Comment on the morphology of the red blood cells.
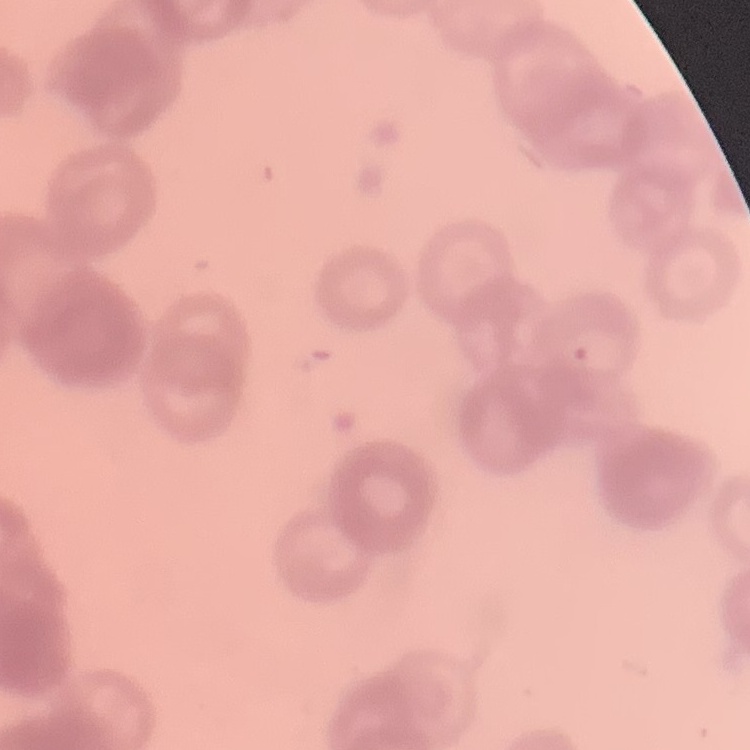

They show rouleaux formation.

Summary:
  - Image type: square crop of a larger photomicrograph
  - Stain: Field's or Giemsa
  - Preparation: thin blood smear